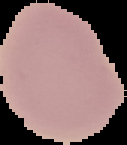

image type = segmented cell region on a black background
preparation = thin blood smear
image size = 127×145 pixels
malaria status = uninfected